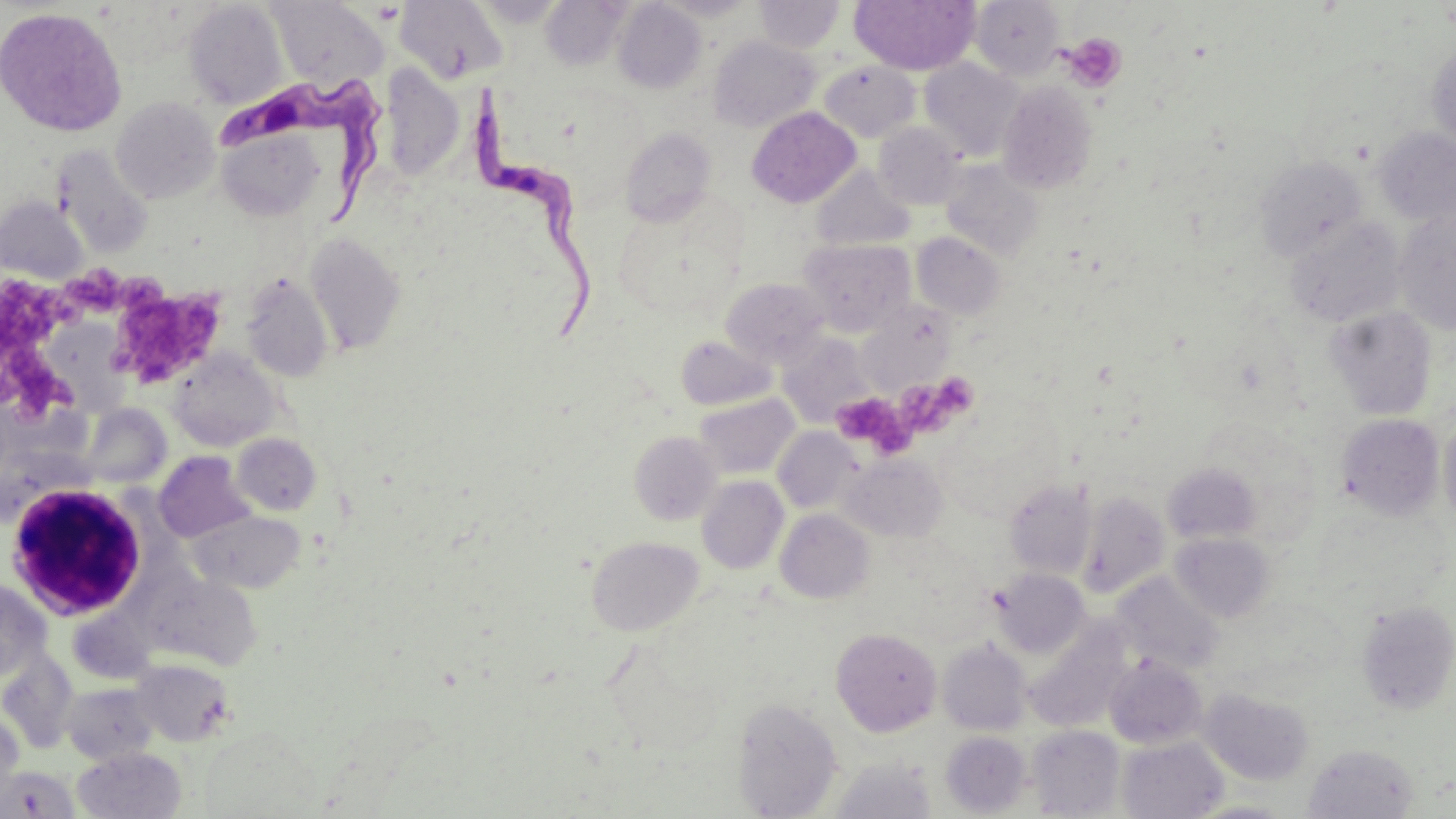
Approximate bounding boxes as named x1/y1/x2/y2 corners in pixels. Uninfected red blood cell locations: (x1=395, y1=0, x2=508, y2=85), (x1=540, y1=0, x2=629, y2=70), (x1=849, y1=0, x2=980, y2=75), (x1=970, y1=0, x2=1066, y2=80), (x1=183, y1=1, x2=288, y2=109), (x1=270, y1=1, x2=387, y2=87), (x1=613, y1=1, x2=706, y2=94), (x1=755, y1=1, x2=844, y2=53), (x1=0, y1=7, x2=127, y2=136), (x1=709, y1=36, x2=820, y2=132), (x1=1427, y1=43, x2=1456, y2=154), (x1=919, y1=58, x2=1025, y2=162), (x1=819, y1=60, x2=921, y2=142), (x1=380, y1=67, x2=464, y2=179), (x1=997, y1=81, x2=1099, y2=195), (x1=111, y1=96, x2=220, y2=204), (x1=747, y1=107, x2=860, y2=208), (x1=874, y1=122, x2=964, y2=209), (x1=620, y1=128, x2=716, y2=227), (x1=1373, y1=128, x2=1456, y2=225), (x1=217, y1=130, x2=325, y2=222), (x1=52, y1=145, x2=154, y2=258), (x1=1254, y1=156, x2=1367, y2=260), (x1=941, y1=160, x2=1044, y2=261), (x1=812, y1=167, x2=913, y2=252), (x1=0, y1=196, x2=88, y2=284), (x1=1394, y1=210, x2=1456, y2=333), (x1=1285, y1=216, x2=1406, y2=327), (x1=305, y1=232, x2=407, y2=355), (x1=912, y1=232, x2=1005, y2=319), (x1=799, y1=238, x2=915, y2=335), (x1=242, y1=275, x2=332, y2=381), (x1=720, y1=277, x2=830, y2=368), (x1=863, y1=302, x2=956, y2=391), (x1=1326, y1=306, x2=1437, y2=420), (x1=777, y1=333, x2=873, y2=424), (x1=675, y1=334, x2=777, y2=410), (x1=169, y1=351, x2=281, y2=451), (x1=694, y1=392, x2=799, y2=480), (x1=78, y1=403, x2=171, y2=489), (x1=1336, y1=413, x2=1445, y2=520), (x1=1439, y1=415, x2=1456, y2=529), (x1=772, y1=427, x2=862, y2=514), (x1=629, y1=431, x2=723, y2=525), (x1=232, y1=433, x2=322, y2=515), (x1=155, y1=452, x2=254, y2=542), (x1=839, y1=453, x2=947, y2=542), (x1=1162, y1=461, x2=1263, y2=545), (x1=696, y1=476, x2=789, y2=574), (x1=1003, y1=477, x2=1096, y2=580), (x1=1077, y1=492, x2=1170, y2=598), (x1=775, y1=509, x2=874, y2=604), (x1=188, y1=510, x2=305, y2=594), (x1=1170, y1=532, x2=1276, y2=622), (x1=586, y1=535, x2=703, y2=636), (x1=992, y1=568, x2=1091, y2=658), (x1=169, y1=570, x2=257, y2=666), (x1=1111, y1=572, x2=1224, y2=674), (x1=0, y1=579, x2=51, y2=680), (x1=1355, y1=600, x2=1455, y2=715), (x1=1023, y1=625, x2=1130, y2=733), (x1=831, y1=627, x2=942, y2=736), (x1=937, y1=639, x2=1032, y2=735), (x1=0, y1=651, x2=80, y2=754), (x1=1104, y1=654, x2=1208, y2=749), (x1=132, y1=660, x2=234, y2=747), (x1=62, y1=682, x2=159, y2=764), (x1=1200, y1=687, x2=1314, y2=786), (x1=733, y1=698, x2=843, y2=818), (x1=0, y1=712, x2=24, y2=806), (x1=1027, y1=725, x2=1124, y2=817), (x1=940, y1=730, x2=1032, y2=817), (x1=1118, y1=736, x2=1228, y2=818), (x1=1302, y1=743, x2=1420, y2=819), (x1=73, y1=747, x2=186, y2=819), (x1=829, y1=758, x2=937, y2=819), (x1=0, y1=765, x2=79, y2=817), (x1=1184, y1=799, x2=1296, y2=818). Trypanosoma brucei locations: (x1=222, y1=77, x2=385, y2=226), (x1=472, y1=88, x2=601, y2=341). Platelet locations: (x1=1061, y1=33, x2=1128, y2=93), (x1=74, y1=265, x2=134, y2=318), (x1=1, y1=279, x2=84, y2=345), (x1=113, y1=286, x2=228, y2=389), (x1=0, y1=341, x2=75, y2=423), (x1=904, y1=379, x2=977, y2=444), (x1=831, y1=391, x2=913, y2=456). White blood cell locations: (x1=2, y1=480, x2=157, y2=620). Slide-level diagnosis: Trypanosoma brucei. Image is 1456×819 pixels. One field of a larger specimen. Captured at 1000x magnification. Light microscopy. May-Grünwald-Giemsa-stained preparation. Thin blood film.